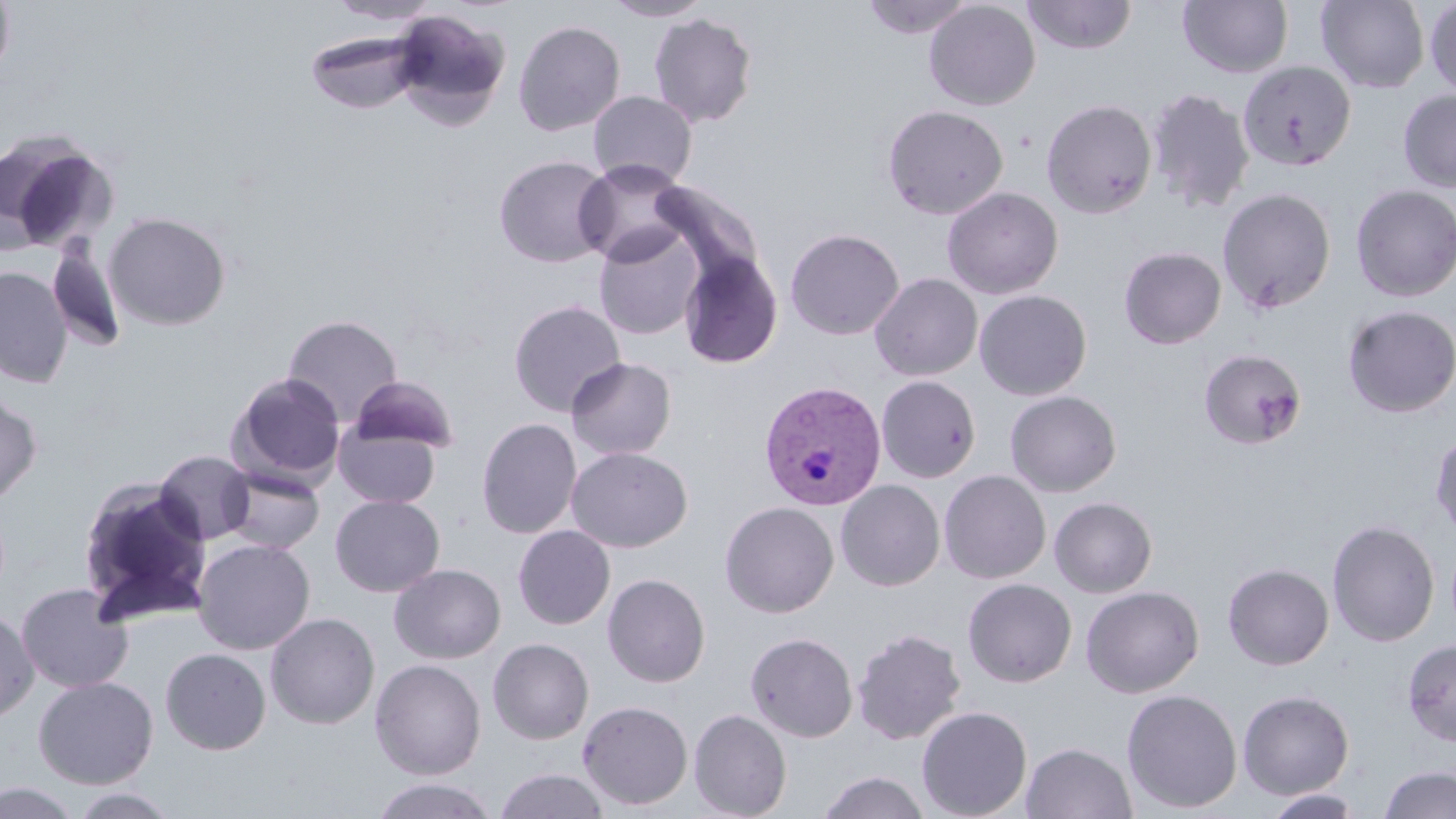

slide-level diagnosis = Plasmodium vivax
modality = optical microscopy
Plasmodium vivax-infected red blood cell locations = approximate bounding boxes as [x1, y1, x2, y2] in pixels: [759, 381, 886, 512]
magnification = 1000x
stain = May-Grünwald-Giemsa
uninfected red blood cell locations = approximate bounding boxes as [x1, y1, x2, y2] in pixels: [0, 0, 16, 83], [601, 0, 715, 21], [861, 0, 976, 38], [1022, 0, 1137, 54], [1315, 0, 1430, 92], [328, 1, 441, 26], [923, 1, 1040, 111], [1178, 1, 1293, 78], [1424, 1, 1456, 98], [390, 9, 512, 128], [649, 13, 758, 128], [513, 20, 626, 136], [304, 28, 428, 114], [1238, 60, 1356, 171], [1145, 88, 1255, 213], [1397, 89, 1456, 193], [588, 91, 698, 189], [1041, 99, 1157, 218], [882, 104, 1008, 219], [0, 129, 119, 254], [493, 154, 614, 268], [573, 158, 693, 267], [649, 179, 765, 285], [1350, 185, 1456, 302], [941, 186, 1063, 299], [1217, 188, 1337, 314], [103, 212, 231, 331], [592, 226, 704, 339], [785, 228, 905, 340], [47, 239, 127, 352], [1118, 247, 1226, 349], [679, 250, 783, 369], [0, 266, 73, 388], [869, 273, 983, 381], [974, 290, 1092, 401], [508, 299, 627, 417], [1342, 305, 1456, 417], [282, 314, 403, 425], [1199, 348, 1306, 450], [566, 357, 677, 460], [228, 372, 346, 486], [348, 375, 460, 454], [876, 375, 981, 483], [1005, 390, 1121, 496], [0, 392, 42, 508], [476, 417, 582, 538], [333, 423, 441, 508], [1430, 429, 1456, 541], [567, 446, 692, 552], [153, 450, 256, 545], [221, 466, 325, 554], [939, 470, 1051, 584], [75, 476, 215, 627], [835, 479, 946, 591], [330, 494, 445, 597], [1049, 497, 1158, 597], [720, 501, 839, 617], [1326, 519, 1440, 647], [513, 525, 615, 629], [192, 538, 315, 655], [1222, 562, 1334, 670], [389, 563, 506, 664], [603, 573, 710, 687], [962, 578, 1077, 687], [16, 582, 134, 693], [1081, 585, 1204, 698], [0, 606, 39, 724], [265, 612, 380, 729], [852, 628, 967, 745], [745, 632, 859, 743], [488, 637, 594, 744], [1402, 638, 1456, 747], [160, 647, 271, 755], [370, 659, 486, 780], [33, 675, 158, 789], [1122, 689, 1243, 813], [1237, 689, 1355, 800], [577, 700, 693, 811], [916, 706, 1032, 818], [688, 708, 792, 819], [1020, 742, 1137, 819], [1380, 764, 1456, 819], [493, 768, 610, 819], [817, 770, 931, 819], [367, 778, 501, 819], [0, 782, 84, 819], [64, 787, 183, 818], [1262, 789, 1367, 818]
preparation = thin blood film
field of view = single
image size = 1456×819 pixels